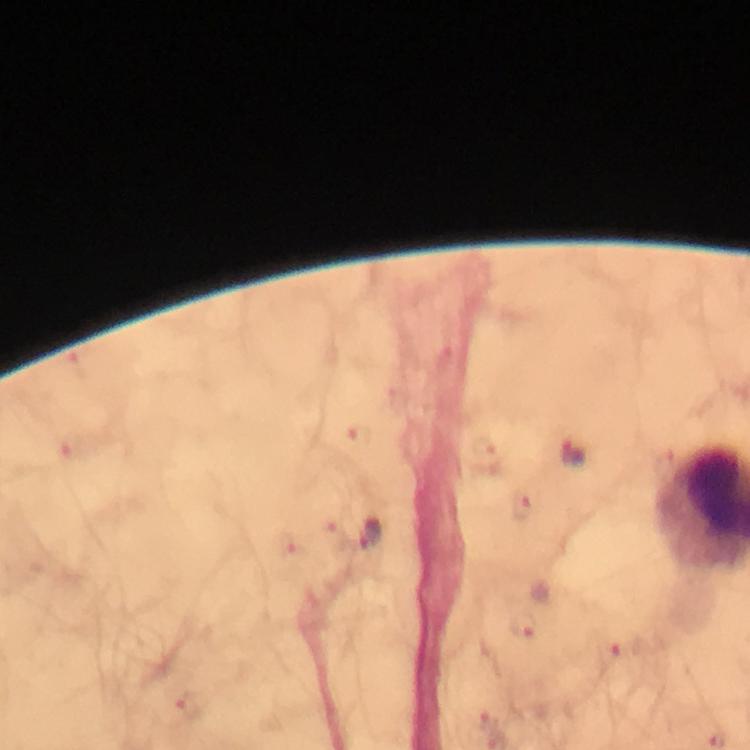

preparation = thick blood smear
malaria parasite locations = approximate centers as [x, y] in pixels: [574, 452], [371, 534], [523, 626], [192, 706], [488, 720]
magnification = 100x
stain = Giemsa
capture = smartphone photograph through a microscope
cropped from = one field of view
immersion oil = applied
context = from a malaria diagnostic workup
image size = 750×750 pixels